Locate every malaria parasite.
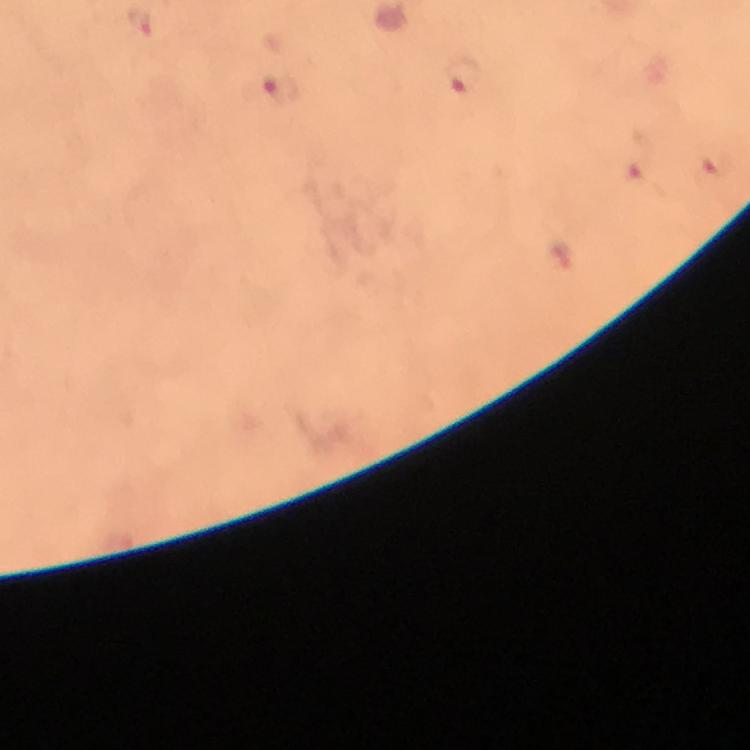

Approximate object centers, in pixels from the top-left corner.
Malaria parasites: (x=140, y=21), (x=465, y=77), (x=280, y=90), (x=712, y=167), (x=635, y=173), (x=563, y=261).

stain: Giemsa
cropped_from: a single field of view
context: from a diagnostic examination for malaria
capture: smartphone mounted on the microscope
immersion_oil: used
magnification: 100x
image_size: 750×750 pixels
preparation: thick blood smear